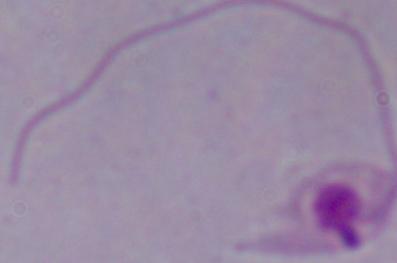

Summary:
  - Identification: Leishmania
  - Magnification: 1000x
  - Modality: micrograph